Locate and identify every blood parasite.
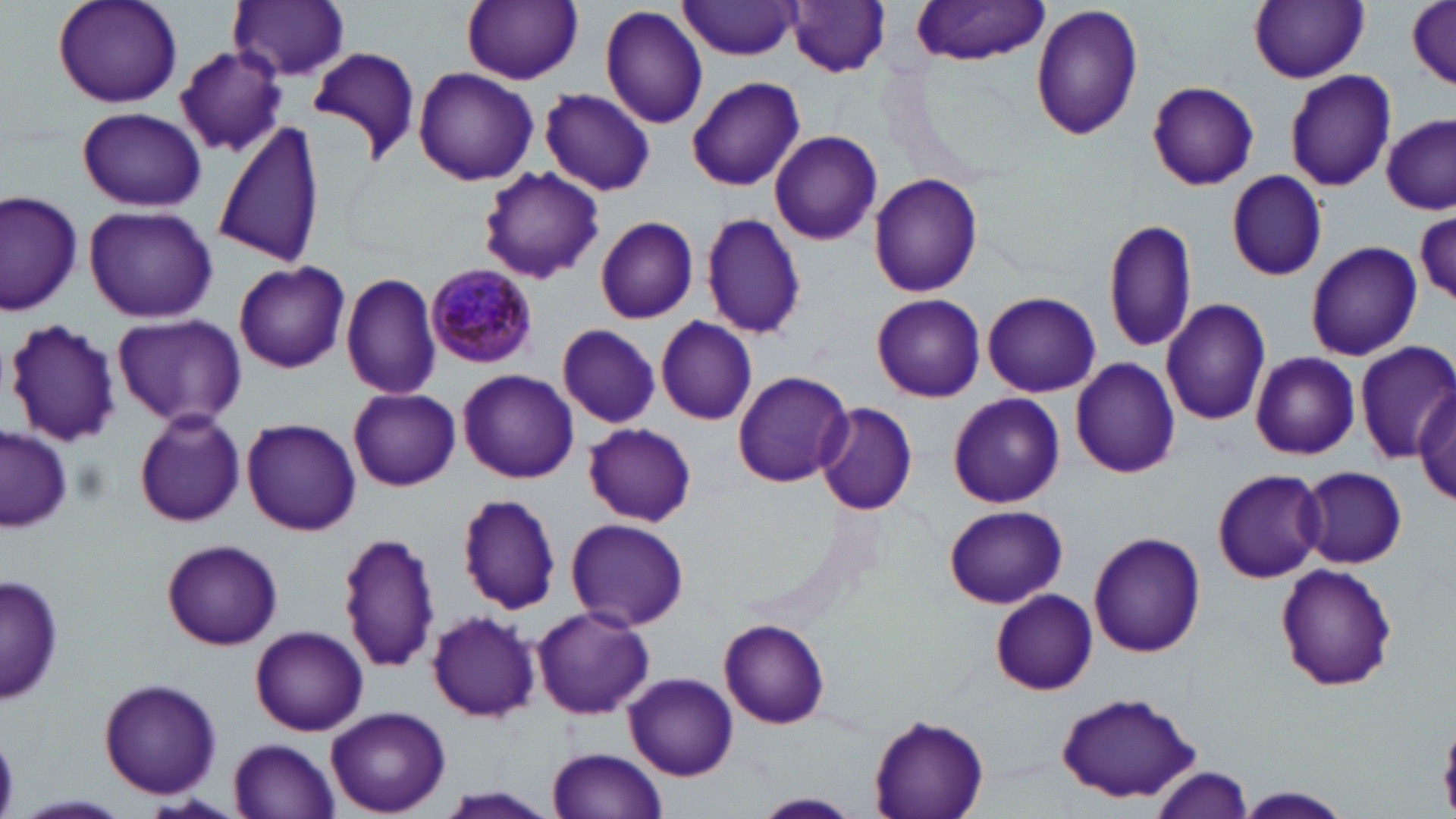

Approximate bounding boxes as (x1,y1)-(x2,y2) corner pairs in pixels.
Plasmodium malariae-infected red blood cells: (427,265)-(537,366).
No Plasmodium falciparum, Plasmodium ovale, Plasmodium vivax, Babesia divergens, or Trypanosoma brucei observed.

{
  "slide_level_diagnosis": "Plasmodium malariae",
  "magnification": "1000x",
  "field_of_view": "one of a larger specimen",
  "preparation": "thin blood film",
  "modality": "light microscopy",
  "uninfected_red_blood_cell_locations": "approximate bounding boxes as (x1,y1)-(x2,y2) corner pairs in pixels: (52,0)-(183,108), (228,0)-(352,81), (461,0)-(583,85), (1249,0)-(1369,83), (1407,0)-(1456,89), (788,1)-(891,77), (677,2)-(799,63), (908,2)-(1052,66), (1029,3)-(1143,140), (600,5)-(711,130), (308,44)-(422,164), (173,45)-(290,158), (1284,68)-(1397,192), (413,69)-(537,185), (687,75)-(805,192), (1147,80)-(1260,190), (419,88)-(582,234), (540,89)-(655,195), (76,105)-(207,211), (1380,114)-(1454,214), (214,120)-(326,270), (769,131)-(883,246), (477,167)-(604,284), (1226,171)-(1328,281), (869,172)-(982,296), (1,189)-(83,316), (82,204)-(219,322), (1414,210)-(1455,306), (700,212)-(807,340), (594,216)-(700,325), (1102,217)-(1199,355), (1306,242)-(1422,360), (233,259)-(351,373), (341,272)-(443,400), (983,291)-(1101,397), (871,294)-(986,401), (1161,298)-(1271,426), (110,313)-(246,429), (655,317)-(757,425), (5,319)-(122,447), (556,324)-(661,428), (659,335)-(822,448), (1353,341)-(1456,463), (1249,352)-(1359,459), (1069,358)-(1181,477), (459,369)-(580,483), (733,370)-(852,486), (1412,382)-(1455,506), (348,387)-(462,491), (948,392)-(1064,509), (816,399)-(918,516), (133,409)-(247,528), (240,417)-(362,536), (583,423)-(696,527), (1,427)-(75,531), (1212,467)-(1327,584), (1299,467)-(1408,568), (458,494)-(563,613), (944,504)-(1066,607), (565,518)-(689,631), (335,529)-(442,674), (1089,531)-(1205,657), (161,538)-(283,650), (1275,564)-(1398,691), (1,572)-(63,706), (991,589)-(1098,695), (530,604)-(654,718), (425,610)-(541,722), (718,619)-(831,729), (250,625)-(368,736), (625,673)-(738,780), (99,678)-(222,798), (1056,692)-(1205,804), (327,706)-(451,816), (867,713)-(991,819), (230,738)-(341,819), (547,746)-(667,819), (1152,765)-(1253,818), (1229,787)-(1353,818), (753,792)-(863,817), (15,794)-(128,817)",
  "stain": "May-Grünwald-Giemsa",
  "image_size": "1456×819 pixels"
}